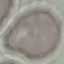
Summary:
  - Malaria status: uninfected
  - Preparation: thin blood smear
  - Image type: automatically extracted cell patch, resized to 64 × 64 pixels
  - Stain: Giemsa
  - Capture: smartphone through the microscope eyepiece